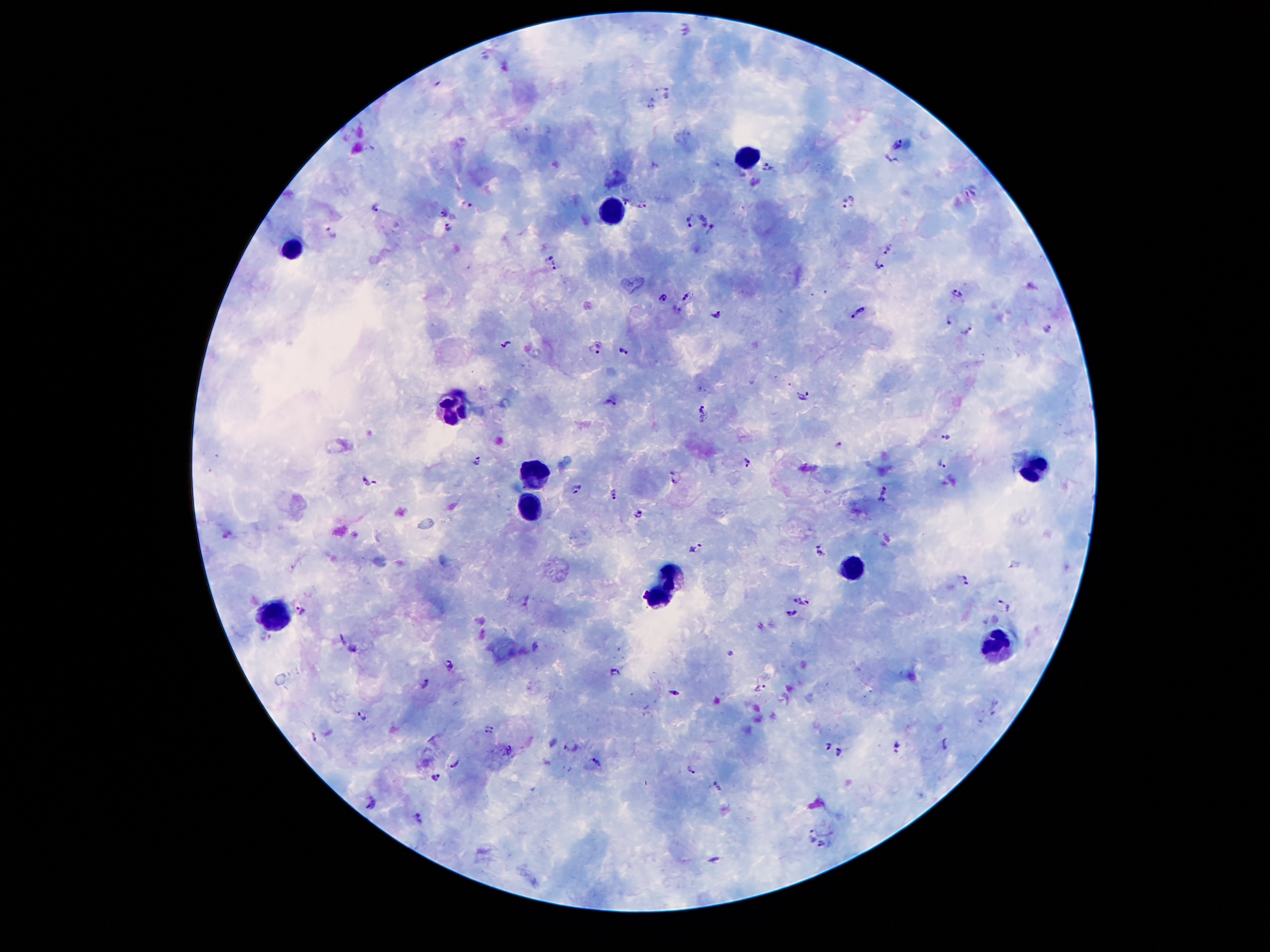

malaria_parasite_locations: 'approximate centers as [x, y] in pixels: [667, 94], [899, 142], [891, 160], [767, 166], [971, 193], [625, 200], [850, 203], [468, 204], [376, 207], [642, 207], [444, 213], [704, 216], [690, 222], [712, 227], [448, 229], [332, 232], [887, 248], [549, 255], [879, 266], [556, 267], [958, 295], [660, 298], [686, 299], [860, 310], [677, 311], [717, 314], [950, 320], [1046, 327], [969, 331], [505, 344], [595, 350], [624, 351], [804, 396], [610, 402], [703, 408], [947, 433], [838, 444], [746, 460], [477, 461], [942, 464], [675, 479], [368, 481], [576, 488], [884, 489], [615, 495], [880, 501], [639, 513], [697, 550], [820, 550], [965, 579], [528, 599], [803, 599], [1007, 606], [301, 609], [792, 614], [760, 626], [265, 635], [344, 639], [536, 647], [354, 649], [729, 653], [450, 662], [617, 671], [426, 682], [760, 688], [674, 694], [362, 716], [489, 729], [313, 736], [828, 744], [944, 745], [898, 746], [571, 747], [509, 750], [839, 753], [596, 761], [456, 763], [691, 770], [437, 777], [718, 787], [371, 803], [419, 819], [813, 833], [822, 844], [714, 859]'
patient_malaria_status: positive for Plasmodium falciparum
capture: smartphone camera through the microscope eyepiece
stain: Giemsa
leukocyte_locations: 'approximate centers as [x, y] in pixels: [741, 154], [610, 206], [291, 247], [453, 410], [1031, 467], [531, 474], [524, 516], [852, 568], [673, 573], [656, 600], [275, 612], [1003, 651]'
field_of_view: single
magnification: 100x
image_size: 1270×952 pixels
preparation: thick peripheral-blood smear